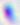
Summary:
  - Magnification: 400x
  - Modality: micrograph
  - Identification: Toxoplasma gondii